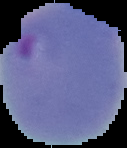

image size = 127×148 pixels
malaria status = parasitized
image type = cell region segmented out of the field of view; surrounding area masked to black
preparation = thin blood film